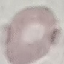

Result: negative for malaria parasites. Automatically extracted cell patch, resized to 64 × 64 pixels. Thin blood smear. Giemsa stain. Acquired by smartphone through the microscope eyepiece.